Classify this cell by malaria status.
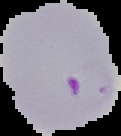
It is parasitized.

image_size: 121×136 pixels
image_type: segmented cell region on a black background
preparation: thin blood smear